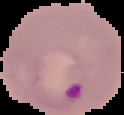

Malaria status: parasitized. From a thin blood film. Image is 124×115 pixels. Segmented cell region on a black background.